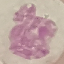 Result: negative for malaria parasites. Giemsa stain. Cell patch, automatically extracted from a larger field of view and resized to 64 × 64 pixels. Thin smear of blood. Photographed with a smartphone camera at the microscope eyepiece.